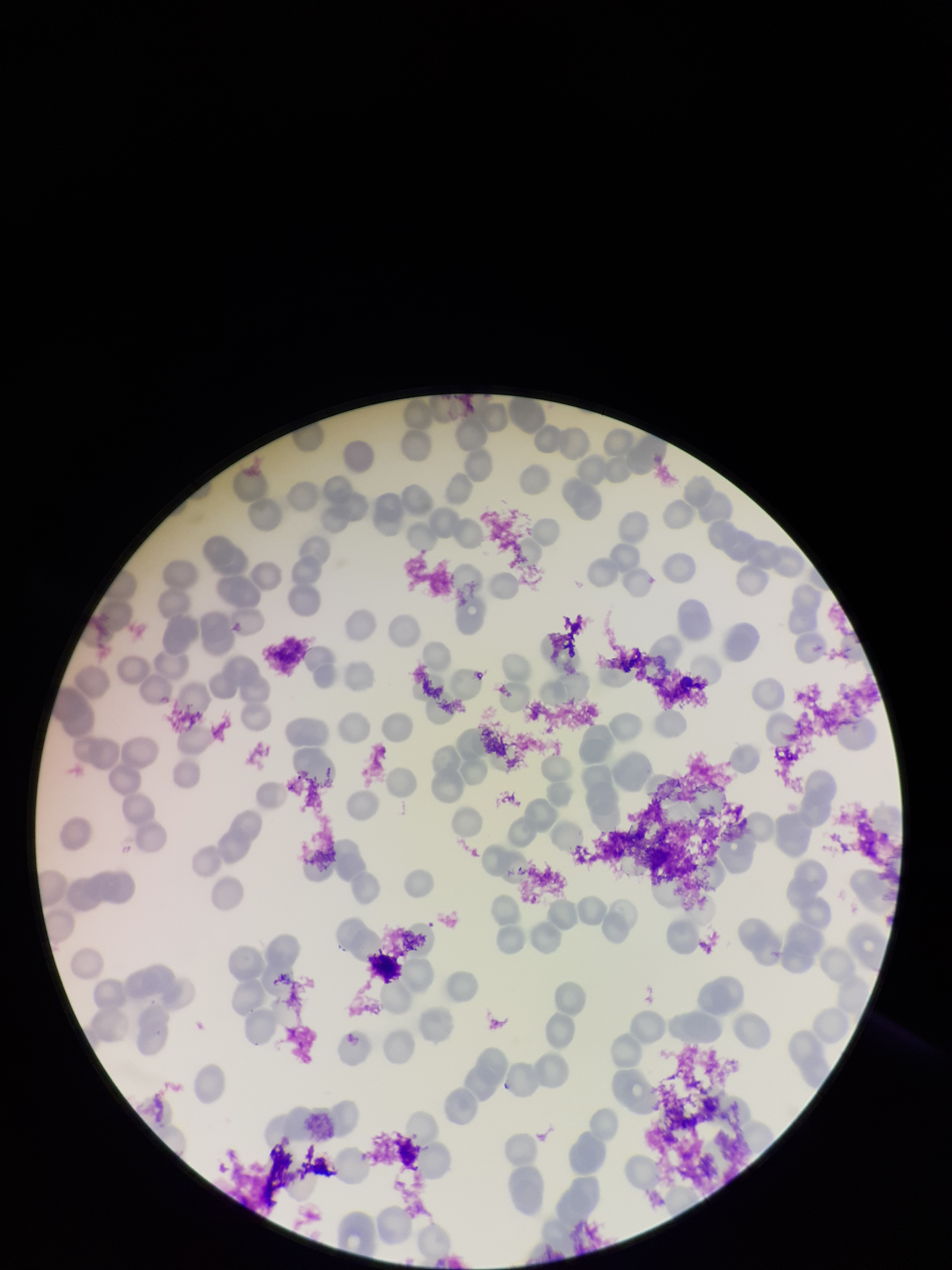
Summary:
  - Capture: smartphone photograph through the microscope eyepiece
  - Patient malaria status: infected
  - Species reported for this patient: Plasmodium falciparum
  - Preparation: thin
  - Parasitized red blood cell count: 0
  - Stain: Giemsa
  - Image size: 952×1270 pixels
  - Parasitized red blood cells: none seen
  - Field of view: one from this slide
  - Red blood cell count: 121